Identify the cell.
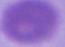

This is an erythrocyte.

Photomicrograph. 1000x magnification.